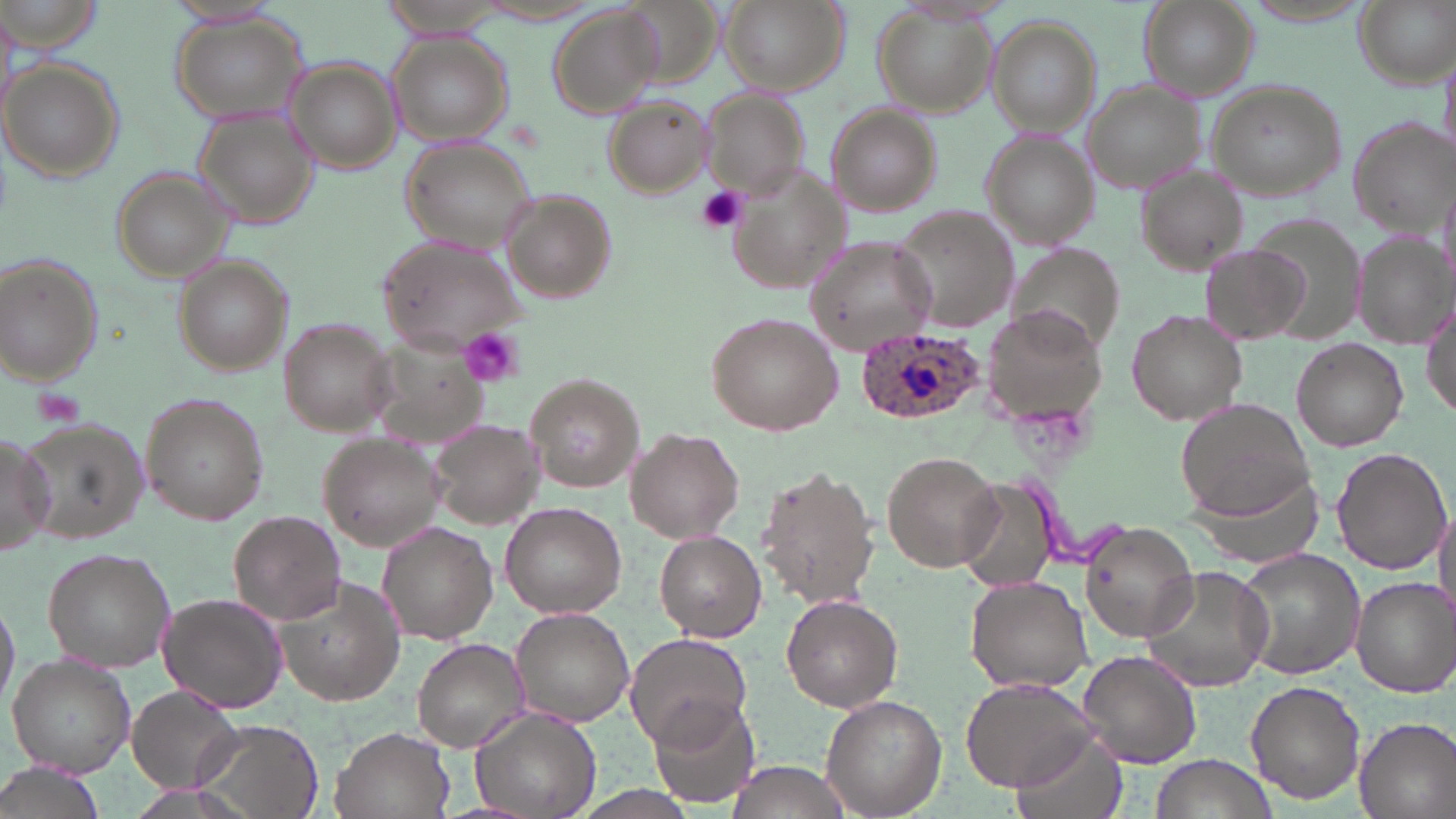

slide-level diagnosis = Plasmodium ovale
image size = 1456×819 pixels
modality = light microscopy
Plasmodium ovale-infected red blood cell locations = approximate bounding boxes as named x1/y1/x2/y2 corners in pixels: (x1=853, y1=327, x2=984, y2=426)
uninfected red blood cell locations = approximate bounding boxes as named x1/y1/x2/y2 corners in pixels: (x1=382, y1=0, x2=510, y2=37), (x1=719, y1=0, x2=846, y2=95), (x1=1138, y1=0, x2=1258, y2=100), (x1=0, y1=2, x2=110, y2=56), (x1=1238, y1=2, x2=1375, y2=28), (x1=1356, y1=2, x2=1453, y2=87), (x1=874, y1=3, x2=998, y2=118), (x1=546, y1=6, x2=664, y2=117), (x1=166, y1=14, x2=310, y2=128), (x1=986, y1=15, x2=1105, y2=137), (x1=386, y1=31, x2=515, y2=147), (x1=284, y1=60, x2=403, y2=172), (x1=0, y1=61, x2=123, y2=182), (x1=1203, y1=80, x2=1348, y2=204), (x1=1084, y1=85, x2=1200, y2=192), (x1=697, y1=89, x2=808, y2=203), (x1=603, y1=94, x2=715, y2=198), (x1=828, y1=103, x2=942, y2=218), (x1=195, y1=108, x2=318, y2=230), (x1=1348, y1=118, x2=1454, y2=232), (x1=979, y1=129, x2=1099, y2=250), (x1=399, y1=138, x2=539, y2=254), (x1=111, y1=165, x2=237, y2=283), (x1=725, y1=165, x2=846, y2=298), (x1=1138, y1=167, x2=1249, y2=273), (x1=504, y1=191, x2=615, y2=303), (x1=893, y1=207, x2=1022, y2=333), (x1=1246, y1=215, x2=1366, y2=344), (x1=1352, y1=232, x2=1452, y2=350), (x1=803, y1=235, x2=936, y2=357), (x1=376, y1=236, x2=525, y2=353), (x1=1199, y1=245, x2=1309, y2=343), (x1=1007, y1=248, x2=1125, y2=356), (x1=1, y1=255, x2=103, y2=386), (x1=175, y1=257, x2=292, y2=373), (x1=1422, y1=295, x2=1456, y2=423), (x1=1127, y1=308, x2=1247, y2=422), (x1=984, y1=309, x2=1104, y2=421), (x1=707, y1=312, x2=845, y2=435), (x1=279, y1=320, x2=400, y2=436), (x1=360, y1=325, x2=491, y2=448), (x1=1292, y1=338, x2=1408, y2=451), (x1=526, y1=373, x2=644, y2=494), (x1=140, y1=391, x2=270, y2=526), (x1=1176, y1=398, x2=1315, y2=519), (x1=14, y1=417, x2=155, y2=544), (x1=429, y1=417, x2=547, y2=531), (x1=627, y1=428, x2=744, y2=541), (x1=0, y1=432, x2=55, y2=557), (x1=316, y1=432, x2=448, y2=550), (x1=1332, y1=447, x2=1452, y2=573), (x1=880, y1=450, x2=1000, y2=571), (x1=1178, y1=459, x2=1321, y2=567), (x1=755, y1=465, x2=880, y2=608), (x1=952, y1=477, x2=1059, y2=593), (x1=499, y1=502, x2=625, y2=618), (x1=1433, y1=504, x2=1455, y2=625), (x1=227, y1=510, x2=346, y2=625), (x1=376, y1=522, x2=499, y2=643), (x1=1079, y1=522, x2=1200, y2=643), (x1=654, y1=532, x2=767, y2=640), (x1=43, y1=547, x2=176, y2=671), (x1=1235, y1=549, x2=1365, y2=682), (x1=1139, y1=565, x2=1275, y2=692), (x1=271, y1=572, x2=408, y2=706), (x1=963, y1=574, x2=1095, y2=693), (x1=1350, y1=577, x2=1456, y2=697), (x1=0, y1=591, x2=18, y2=717), (x1=158, y1=592, x2=288, y2=713), (x1=782, y1=595, x2=903, y2=712), (x1=511, y1=607, x2=635, y2=727), (x1=624, y1=632, x2=750, y2=749), (x1=412, y1=637, x2=527, y2=750), (x1=1075, y1=648, x2=1203, y2=768), (x1=7, y1=654, x2=135, y2=776), (x1=959, y1=675, x2=1098, y2=792), (x1=1245, y1=680, x2=1366, y2=806), (x1=128, y1=685, x2=247, y2=796), (x1=648, y1=695, x2=757, y2=811), (x1=820, y1=695, x2=947, y2=819), (x1=471, y1=710, x2=599, y2=818), (x1=1354, y1=717, x2=1456, y2=819), (x1=192, y1=720, x2=324, y2=819), (x1=331, y1=726, x2=454, y2=819), (x1=1009, y1=731, x2=1127, y2=819), (x1=1151, y1=754, x2=1275, y2=819), (x1=722, y1=759, x2=851, y2=819)
field of view = single
stain = May-Grünwald-Giemsa
magnification = 1000x
preparation = thin blood film
platelet locations = approximate bounding boxes as named x1/y1/x2/y2 corners in pixels: (x1=695, y1=185, x2=750, y2=234), (x1=457, y1=327, x2=527, y2=388)